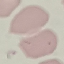

Summary:
  - Malaria status: uninfected
  - Image type: automatically extracted cell patch, resized to 64 × 64 pixels
  - Stain: Giemsa
  - Preparation: thin blood smear
  - Capture: smartphone through the microscope eyepiece